Report the malaria status of this cell.
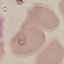

It is uninfected.

Summary:
  - Capture: smartphone through the microscope eyepiece
  - Stain: Giemsa
  - Image type: automatically extracted cell patch, resized to 64 × 64 pixels
  - Preparation: thin blood film